Locate every leukocyte (white blood cell).
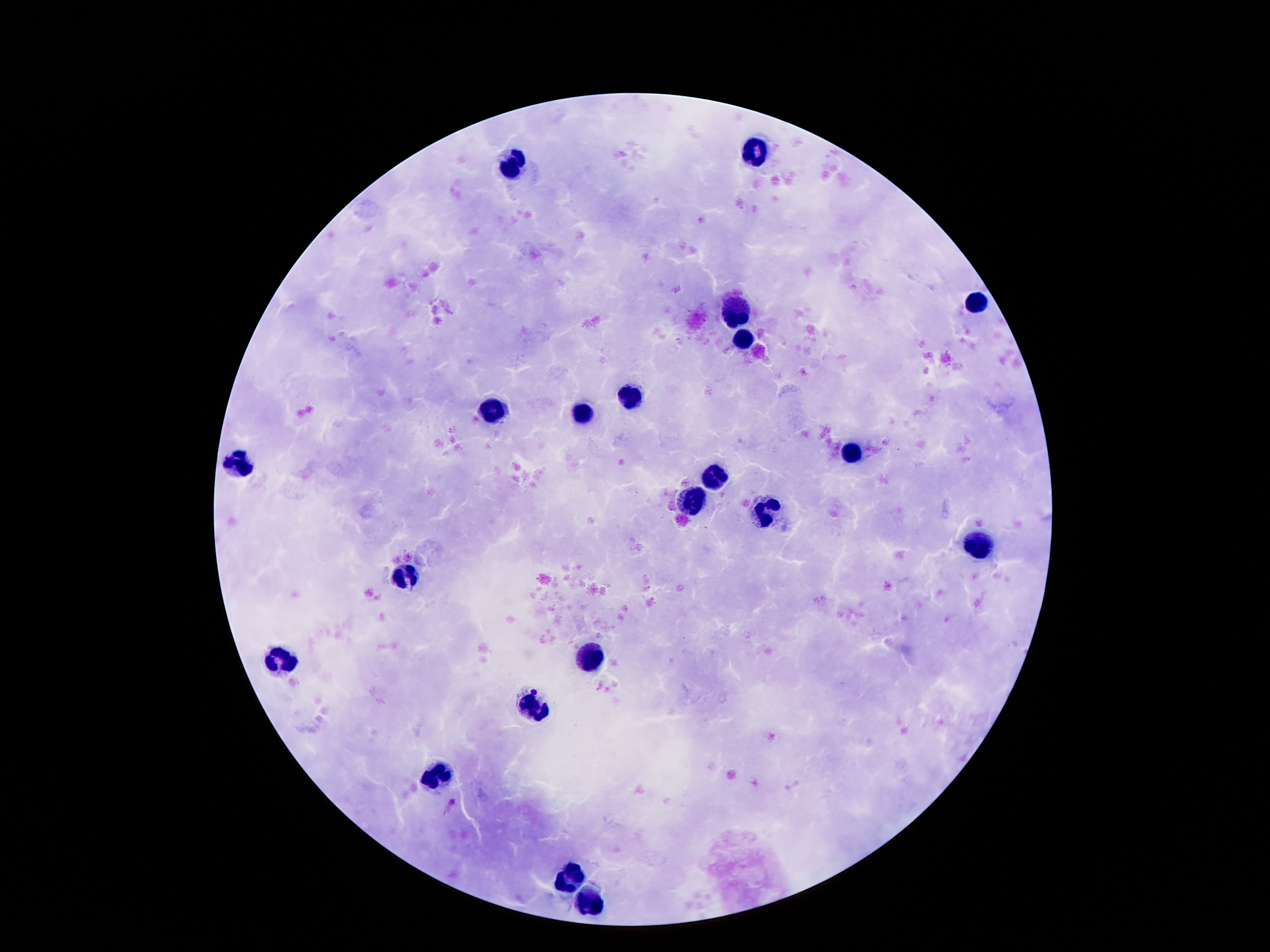
Approximate centers as {x, y} in pixels.
Leukocytes: {755, 150}, {517, 161}, {976, 305}, {736, 310}, {744, 336}, {630, 398}, {492, 412}, {581, 414}, {851, 453}, {236, 465}, {714, 478}, {693, 501}, {767, 513}, {978, 545}, {404, 576}, {591, 656}, {279, 660}, {536, 705}, {437, 775}, {566, 879}, {585, 903}.

Summary:
  - Magnification: 100x
  - Image size: 1270×952 pixels
  - Patient malaria status: uninfected
  - Stain: Giemsa
  - Preparation: thick blood film
  - Field of view: single
  - Capture: smartphone camera through the microscope eyepiece